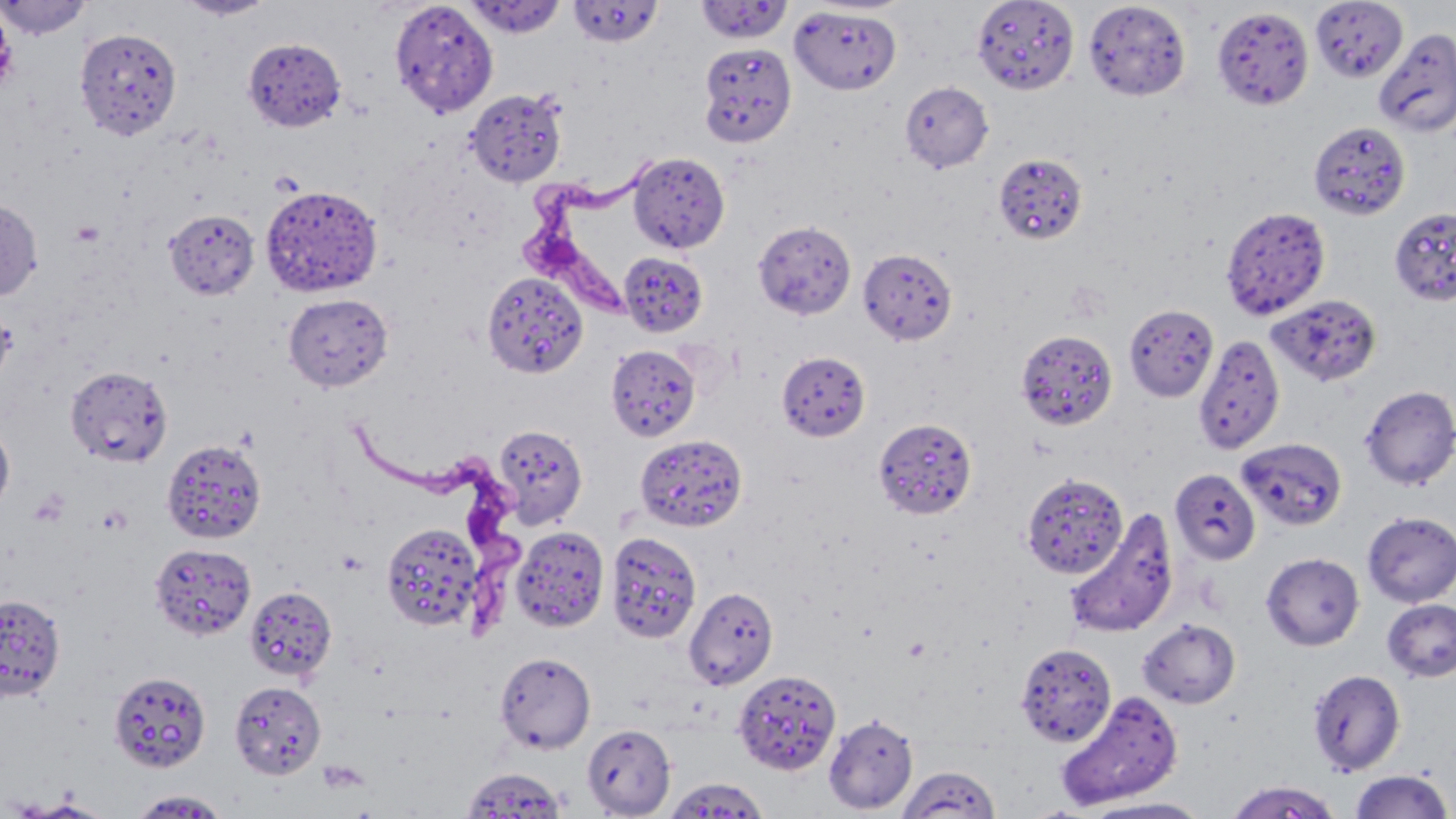
slide-level diagnosis = Trypanosoma brucei
image size = 1456×819 pixels
Trypanosoma brucei locations = approximate bounding boxes as (x1,y1)-(x2,y2) corner pairs in pixels: (521,163)-(657,314), (350,420)-(525,636)
magnification = 1000x
platelet locations = approximate bounding boxes as (x1,y1)-(x2,y2) corner pairs in pixels: (71,219)-(104,246)
modality = optical microscopy
uninfected red blood cell locations = approximate bounding boxes as (x1,y1)-(x2,y2) corner pairs in pixels: (0,0)-(91,39), (176,0)-(277,20), (389,0)-(498,118), (465,0)-(565,38), (971,0)-(1080,95), (1310,0)-(1407,83), (568,1)-(664,47), (695,1)-(794,44), (1082,1)-(1191,101), (789,6)-(902,94), (1212,6)-(1314,110), (0,7)-(15,94), (75,27)-(182,141), (1374,28)-(1456,138), (243,37)-(347,131), (698,41)-(797,147), (900,81)-(993,173), (465,88)-(568,186), (1308,122)-(1410,220), (628,151)-(730,253), (993,152)-(1088,245), (261,185)-(382,297), (0,198)-(43,301), (1221,205)-(1331,320), (164,208)-(260,300), (1393,210)-(1455,308), (753,219)-(856,320), (857,248)-(957,345), (619,250)-(708,336), (482,271)-(588,379), (282,293)-(394,392), (1267,294)-(1382,387), (1124,304)-(1218,402), (1017,328)-(1119,431), (1193,333)-(1285,455), (605,344)-(700,442), (776,351)-(871,441), (65,365)-(173,468), (1360,384)-(1456,490), (874,418)-(976,519), (0,421)-(15,514), (492,424)-(588,529), (634,433)-(748,533), (1237,437)-(1348,531), (162,438)-(267,543), (1170,469)-(1260,565), (1022,472)-(1128,579), (1064,510)-(1179,640), (1362,511)-(1456,607), (381,523)-(483,630), (510,526)-(610,632), (606,531)-(702,644), (150,543)-(256,640), (1261,552)-(1364,651), (244,585)-(337,682), (684,586)-(778,689), (0,594)-(66,699), (1382,599)-(1456,682), (1138,618)-(1240,709), (1014,643)-(1117,747), (495,651)-(596,754), (1307,668)-(1406,776), (733,669)-(841,775), (109,670)-(211,772), (229,680)-(327,779), (1056,691)-(1183,810), (823,714)-(918,814), (581,723)-(676,817), (897,765)-(1002,818), (460,767)-(569,817), (1348,770)-(1454,819), (664,776)-(769,818), (1225,779)-(1342,818), (128,789)-(231,817), (1084,796)-(1213,818)
preparation = thin blood smear
field of view = single
stain = May-Grünwald-Giemsa